State which parasite is depicted.
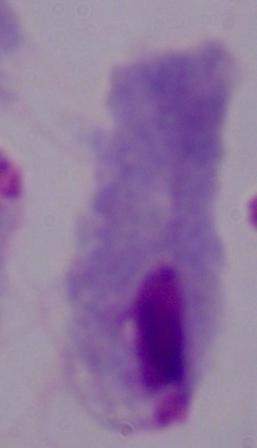

A trichomonad.

Summary:
  - Modality: photomicrograph
  - Magnification: 1000x